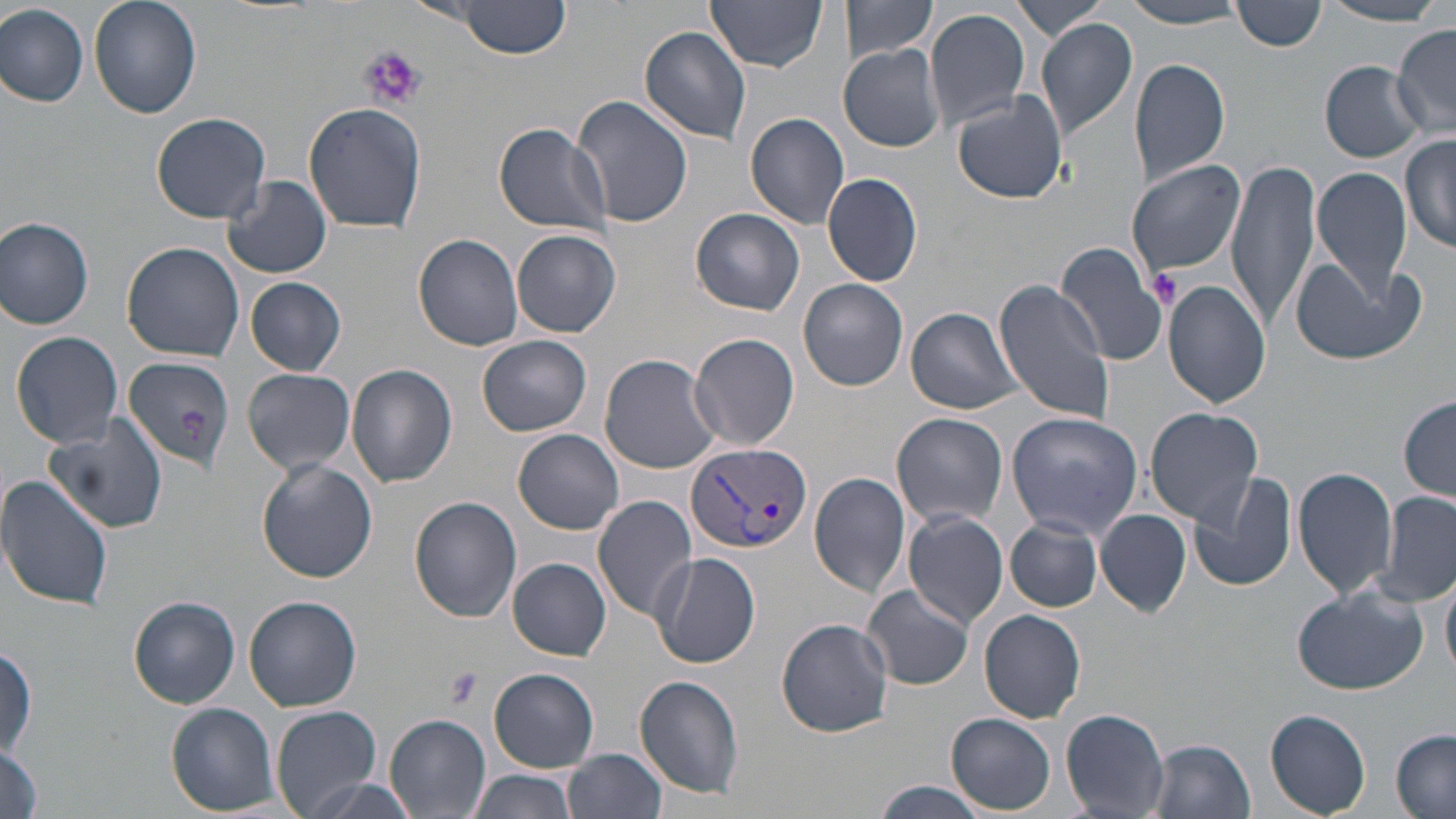
Approximate bounding boxes as (x1, y1, x2, y2) in pixels. Uninfected red blood cell locations: (89, 0, 202, 119), (453, 0, 571, 58), (706, 0, 826, 73), (841, 0, 938, 61), (1010, 0, 1108, 41), (1233, 1, 1326, 52), (1121, 2, 1253, 28), (1317, 3, 1448, 25), (0, 4, 90, 107), (925, 8, 1030, 134), (1035, 19, 1139, 141), (1391, 25, 1456, 134), (639, 26, 753, 144), (839, 44, 945, 152), (1129, 58, 1231, 188), (1319, 62, 1425, 161), (953, 92, 1068, 203), (573, 96, 694, 231), (303, 102, 427, 232), (152, 111, 272, 223), (745, 112, 850, 229), (494, 122, 614, 237), (1401, 134, 1456, 254), (1127, 159, 1245, 276), (1226, 160, 1322, 333), (1312, 168, 1414, 301), (822, 172, 924, 287), (222, 176, 333, 279), (691, 209, 805, 316), (0, 217, 96, 329), (512, 229, 620, 338), (413, 234, 525, 351), (121, 241, 244, 361), (1055, 242, 1168, 366), (1289, 257, 1423, 367), (245, 277, 347, 375), (994, 278, 1115, 426), (799, 279, 909, 391), (1164, 279, 1270, 409), (905, 307, 1023, 415), (10, 331, 124, 450), (689, 333, 800, 451), (478, 335, 593, 435), (599, 353, 723, 474), (121, 356, 233, 473), (347, 363, 458, 487), (242, 368, 356, 473), (1399, 397, 1456, 500), (1145, 407, 1263, 526), (1005, 411, 1143, 539), (47, 412, 170, 535), (892, 412, 1008, 528), (14, 425, 153, 593), (513, 429, 625, 536), (257, 459, 379, 584), (1294, 465, 1398, 599), (1187, 470, 1298, 594), (809, 472, 911, 596), (0, 473, 116, 612), (1378, 491, 1456, 606), (592, 494, 698, 619), (410, 496, 522, 622), (1096, 508, 1190, 618), (901, 512, 1009, 631), (1006, 518, 1103, 612), (651, 553, 760, 669), (508, 558, 611, 659), (1441, 568, 1456, 681), (862, 584, 976, 690), (1291, 585, 1426, 696), (243, 595, 361, 711), (129, 596, 240, 709), (979, 609, 1086, 723), (777, 618, 894, 738), (490, 668, 599, 772), (634, 674, 745, 799), (166, 702, 279, 815), (271, 705, 383, 816), (1061, 708, 1171, 816), (1262, 708, 1371, 816), (947, 712, 1057, 813), (385, 715, 491, 819), (1391, 730, 1456, 817), (1147, 737, 1257, 818), (3, 742, 42, 819), (565, 749, 666, 819), (467, 769, 577, 819), (299, 777, 418, 819), (870, 780, 990, 819). Platelet locations: (357, 45, 426, 111), (1148, 268, 1184, 308), (177, 409, 209, 442), (441, 666, 481, 708). Plasmodium vivax-infected red blood cell locations: (685, 440, 811, 555). Slide-level diagnosis: Plasmodium vivax. May-Grünwald-Giemsa-stained preparation. Image is 1456×819 pixels. Light microscopy. Captured at 1000x magnification. Thin blood film. Single field of view.